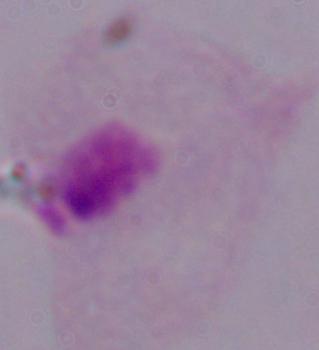
Summary:
  - Modality: micrograph
  - Magnification: 1000x
  - Identification: trichomonad